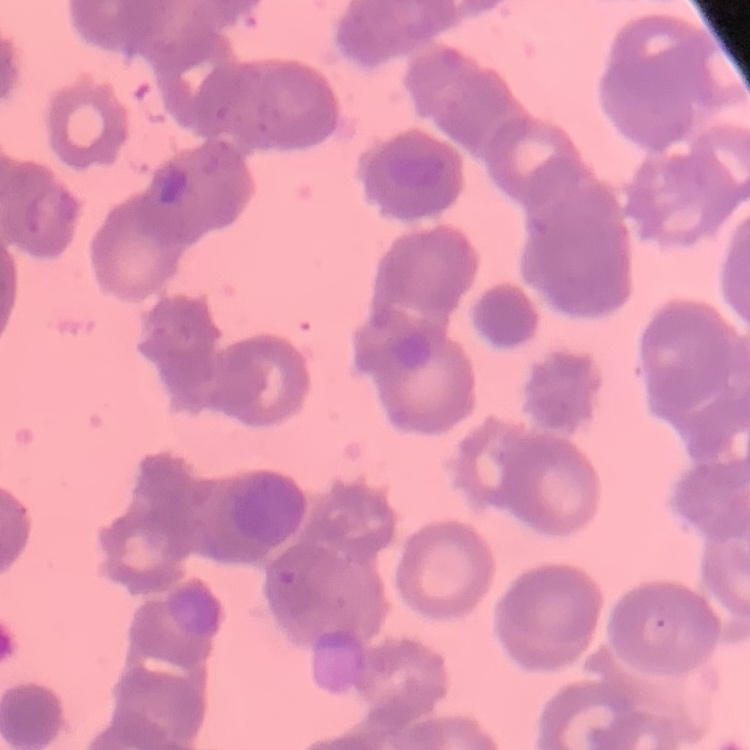
Summary:
  - Erythrocyte morphology: rouleaux formation
  - Image type: square crop of a larger photomicrograph
  - Preparation: thin peripheral smear
  - Stain: Field's or Giemsa